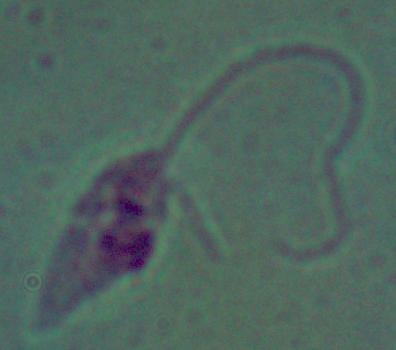
magnification = 1000x
modality = photomicrograph
identification = Leishmania